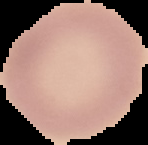

Image is 148×145 pixels. From a thin blood smear. Segmented cell region on a black background. Result: no malaria parasites detected.